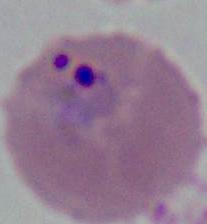

Summary:
  - Modality: micrograph
  - Magnification: 400x or 1000x
  - Identification: Plasmodium